Outline each blood parasite and name the species.
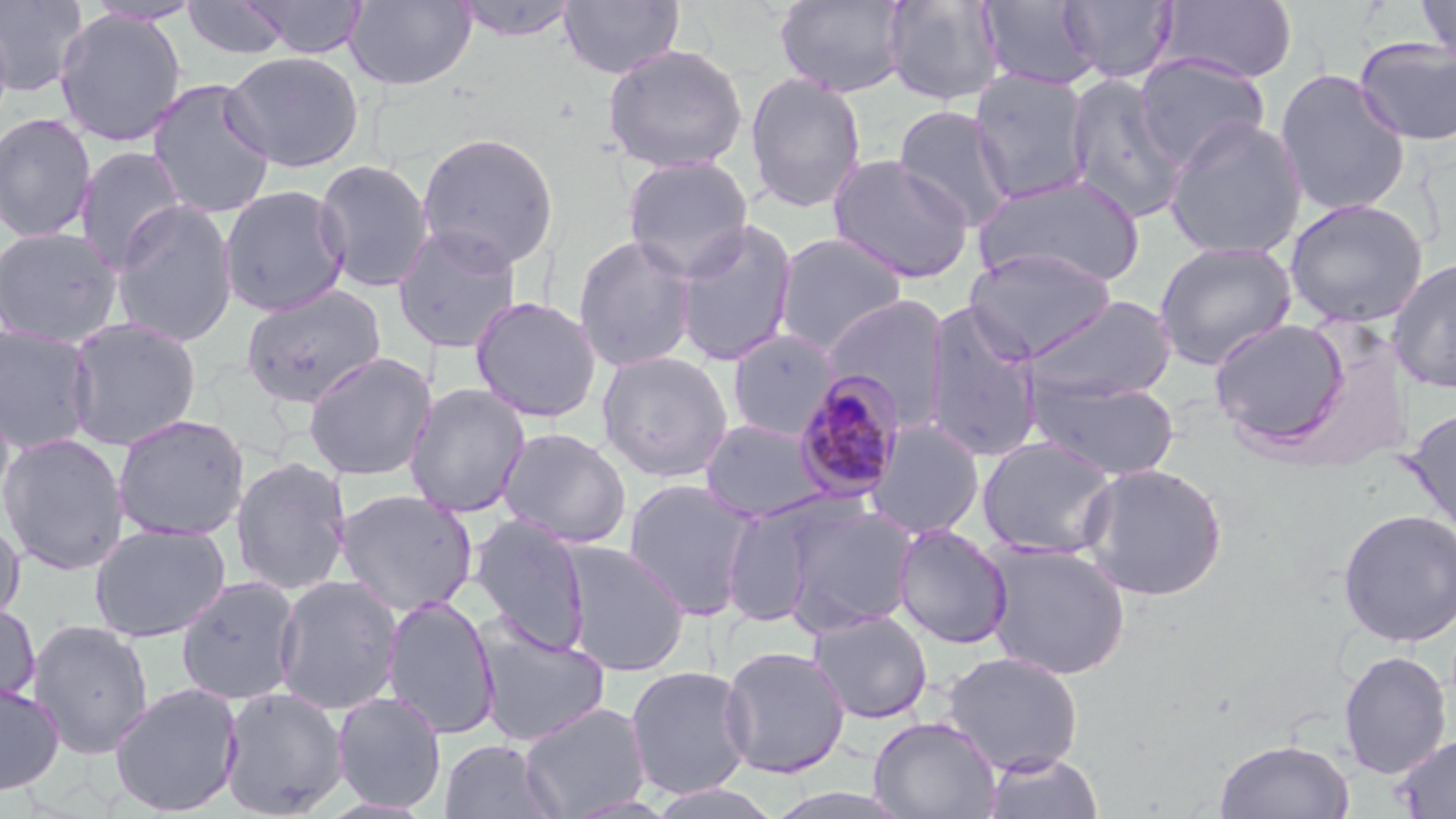

Approximate bounding boxes as (x1,y1)-(x2,y2) corner pairs in pixels.
Plasmodium malariae-infected red blood cells: (793,370)-(907,503).
No Plasmodium falciparum, Plasmodium ovale, Plasmodium vivax, Babesia divergens, or Trypanosoma brucei observed.

Summary:
  - Uninfected red blood cell locations: (0,0)-(88,97), (181,0)-(294,61), (242,0)-(370,60), (344,0)-(476,91), (451,0)-(584,43), (558,0)-(685,79), (774,0)-(912,98), (977,0)-(1101,91), (1416,0)-(1456,65), (84,1)-(204,26), (881,1)-(1005,107), (1059,1)-(1178,84), (1160,1)-(1299,84), (54,8)-(187,147), (0,13)-(14,139), (1353,35)-(1456,146), (602,42)-(749,173), (221,51)-(364,172), (1133,52)-(1271,171), (969,69)-(1094,204), (1274,69)-(1412,217), (745,72)-(867,213), (1063,72)-(1189,223), (147,78)-(276,219), (892,105)-(1015,229), (0,113)-(98,244), (1163,117)-(1307,260), (416,131)-(559,271), (74,146)-(187,272), (827,154)-(975,284), (622,155)-(754,280), (313,158)-(434,293), (973,173)-(1146,289), (219,185)-(351,317), (1284,197)-(1429,328), (110,200)-(239,348), (673,219)-(799,367), (391,223)-(524,353), (0,226)-(124,347), (773,232)-(908,355), (572,233)-(698,373), (1153,241)-(1297,371), (963,247)-(1117,361), (1387,257)-(1456,394), (240,284)-(387,409), (822,294)-(950,427), (469,295)-(603,423), (1025,295)-(1177,404), (922,301)-(1045,464), (63,316)-(202,451), (1210,317)-(1349,444), (0,324)-(98,455), (726,329)-(840,440), (596,350)-(734,483), (302,351)-(437,482), (1026,374)-(1181,481), (403,382)-(532,519), (0,394)-(15,519), (1402,407)-(1456,543), (112,413)-(249,541), (699,418)-(831,522), (864,420)-(985,540), (497,427)-(632,548), (0,431)-(130,576), (977,436)-(1120,559), (230,457)-(352,595), (1078,462)-(1228,601), (622,478)-(758,619), (334,488)-(479,617), (721,502)-(820,628), (785,502)-(918,633), (1337,508)-(1456,647), (468,514)-(591,656), (0,516)-(26,628), (88,522)-(231,642), (893,524)-(1012,650), (560,540)-(691,676), (981,542)-(1132,680), (273,575)-(403,715), (175,576)-(303,706), (381,595)-(501,740), (0,600)-(40,710), (807,609)-(933,724), (27,619)-(155,759), (472,619)-(611,747), (718,645)-(851,779), (1338,649)-(1453,779), (941,651)-(1085,775), (624,665)-(755,800), (0,682)-(64,796), (108,682)-(244,816), (219,685)-(349,819), (331,691)-(446,812), (518,701)-(651,818), (868,715)-(1002,819), (1395,733)-(1456,818), (1214,738)-(1355,818), (439,739)-(562,819), (981,751)-(1104,819), (645,783)-(784,818)
  - Slide-level diagnosis: Plasmodium malariae
  - Magnification: 1000x
  - Modality: optical microscopy
  - Preparation: thin blood film
  - Field of view: single
  - Image size: 1456×819 pixels
  - Stain: May-Grünwald-Giemsa